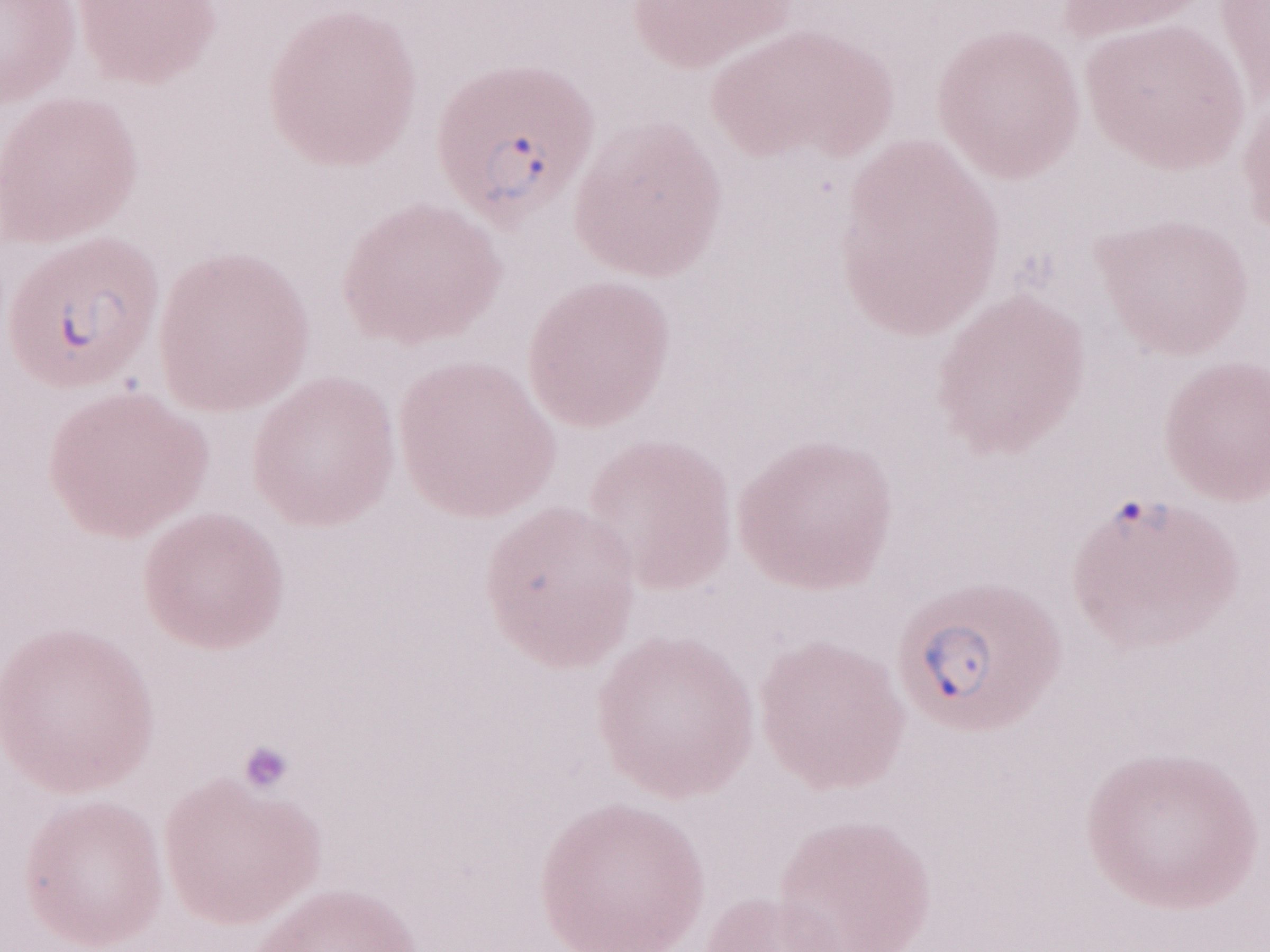 Single field of view. May-Grünwald-Giemsa (MGG) stain. Patient-level malaria diagnosis: positive. Thin blood smear. Olympus BX43 microscope and DP73 digital camera. 1,000x magnification. Image is 1270×952 pixels.